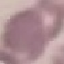

result = negative for malaria parasites
stain = Giemsa
image type = automatically extracted cell patch, resized to 64 × 64 pixels
capture = smartphone camera at the microscope eyepiece
preparation = thin smear